State the preparation type.
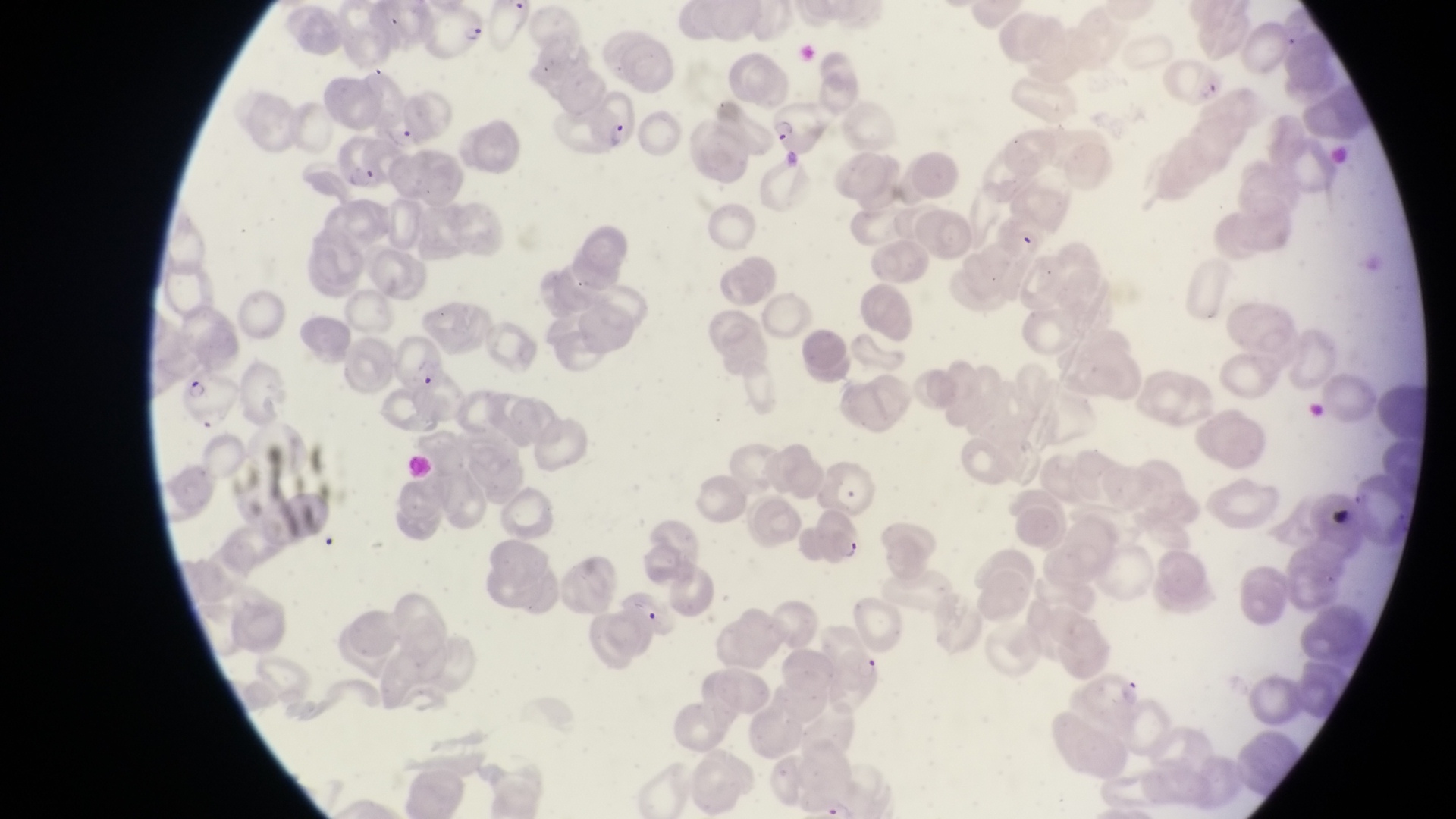
Thin blood smear.

{
  "country": "Uganda",
  "parasitised_red_blood_cell_locations": "approximate bounding boxes as left top right bottom in pixels: 425 6 489 60; 1166 58 1227 108; 589 89 644 158; 770 103 827 158; 337 135 390 190; 389 325 447 392; 184 377 237 427; 814 505 866 560; 835 645 887 706",
  "trophozoite_locations": "approximate bounding boxes as left top right bottom in pixels: 388 125 421 154",
  "image_size": "1456×819 pixels",
  "magnification": "1000x",
  "field_of_view": "single",
  "capture": "smartphone photograph through the eyepiece of an Olympus CX-23 microscope"
}